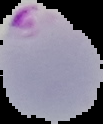

{
  "image_size": "103×124 pixels",
  "preparation": "thin blood film",
  "image_type": "segmented cell region with the area outside set to black",
  "malaria_status": "parasitized"
}